Locate and identify every blood parasite.
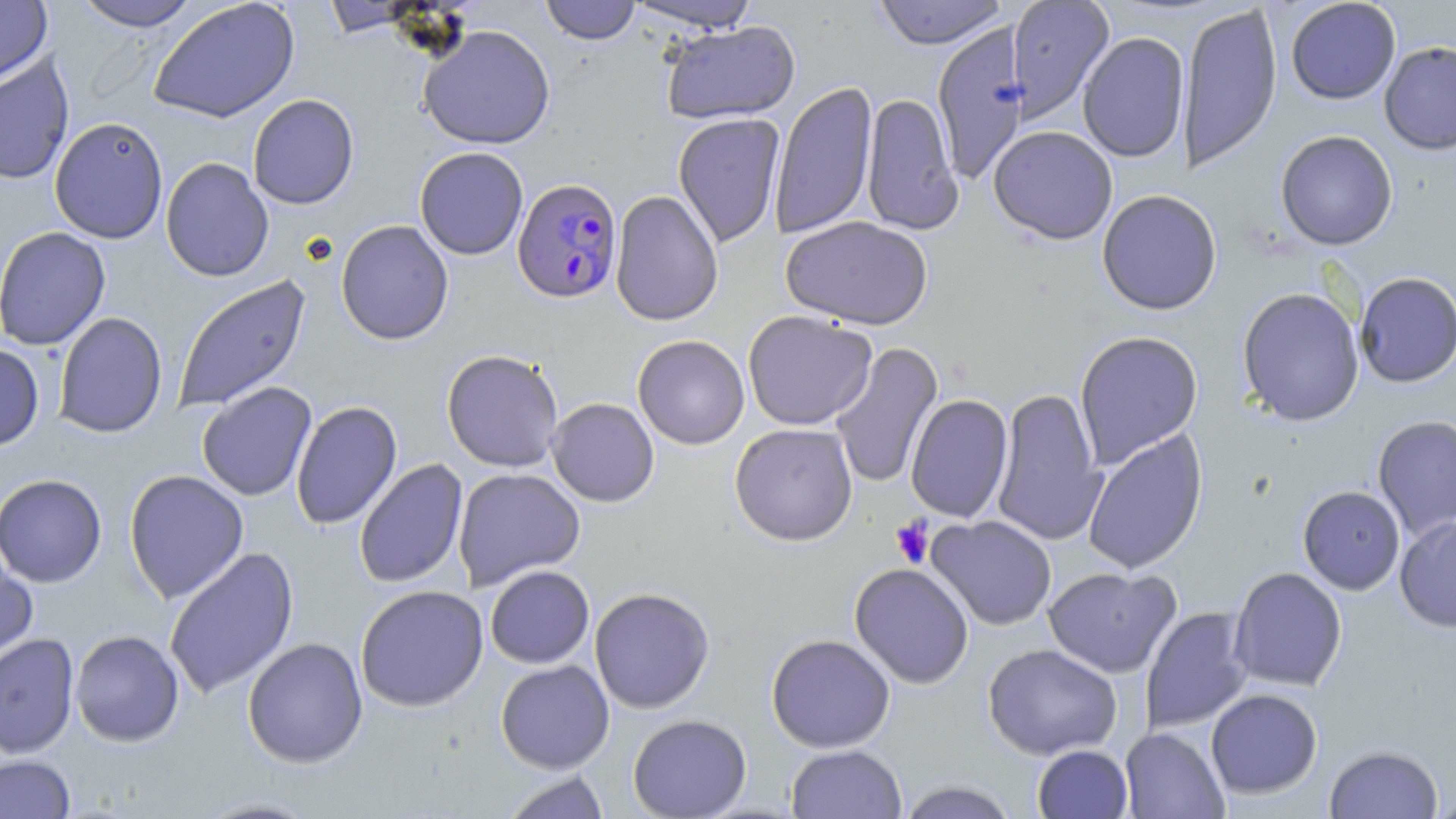

Approximate bounding boxes as (x1, y1, x2, y2) in pixels.
Plasmodium falciparum-infected red blood cells: (512, 178, 623, 304).
No Plasmodium ovale, Plasmodium malariae, Plasmodium vivax, Babesia divergens, or Trypanosoma brucei observed.

Summary:
  - Platelet locations: (890, 516, 934, 568)
  - Uninfected red blood cell locations: (0, 0, 52, 84), (73, 0, 200, 31), (872, 0, 1009, 49), (1006, 0, 1115, 123), (1285, 0, 1401, 105), (148, 1, 300, 123), (321, 1, 419, 37), (540, 1, 641, 45), (624, 1, 761, 32), (1177, 2, 1282, 175), (661, 21, 800, 124), (932, 23, 1031, 186), (418, 25, 556, 150), (1078, 31, 1190, 163), (1379, 41, 1456, 155), (0, 54, 74, 186), (769, 80, 878, 240), (861, 92, 963, 235), (247, 94, 359, 209), (673, 113, 785, 248), (49, 116, 168, 244), (988, 125, 1118, 245), (1275, 130, 1398, 250), (414, 146, 528, 260), (160, 157, 274, 282), (1097, 189, 1222, 315), (609, 190, 723, 327), (780, 216, 934, 330), (335, 220, 454, 345), (0, 226, 111, 351), (1354, 272, 1456, 388), (171, 274, 311, 413), (1236, 286, 1365, 427), (742, 310, 877, 430), (53, 312, 168, 438), (1074, 330, 1204, 469), (632, 335, 750, 449), (829, 341, 944, 490), (0, 343, 45, 451), (441, 349, 564, 472), (197, 382, 317, 502), (991, 386, 1107, 547), (905, 394, 1013, 523), (546, 397, 659, 507), (291, 401, 402, 531), (1372, 415, 1456, 541), (730, 423, 858, 546), (1082, 428, 1208, 575), (353, 458, 468, 589), (452, 467, 586, 591), (124, 469, 249, 603), (0, 473, 107, 588), (1297, 485, 1406, 595), (1394, 514, 1456, 632), (926, 515, 1057, 631), (0, 546, 38, 672), (163, 547, 300, 699), (849, 563, 974, 689), (484, 565, 595, 669), (1043, 566, 1181, 679), (1228, 567, 1347, 692), (355, 584, 489, 712), (589, 587, 715, 713), (1140, 607, 1253, 735), (69, 630, 185, 747), (0, 633, 79, 758), (765, 633, 896, 753), (242, 637, 368, 768), (983, 643, 1123, 760), (495, 660, 615, 774), (1205, 688, 1323, 799), (627, 714, 752, 818), (1120, 727, 1230, 818), (785, 744, 907, 818), (1032, 744, 1133, 818), (1324, 745, 1444, 818), (0, 754, 75, 819), (499, 771, 612, 818), (897, 780, 1019, 818), (1432, 786, 1456, 818), (194, 796, 324, 818)
  - Slide-level diagnosis: Plasmodium falciparum
  - Field of view: single
  - Preparation: thin blood film
  - Stain: May-Grünwald-Giemsa
  - Modality: optical microscopy
  - Image size: 1456×819 pixels
  - Magnification: 1000x